Locate and identify every blood parasite.
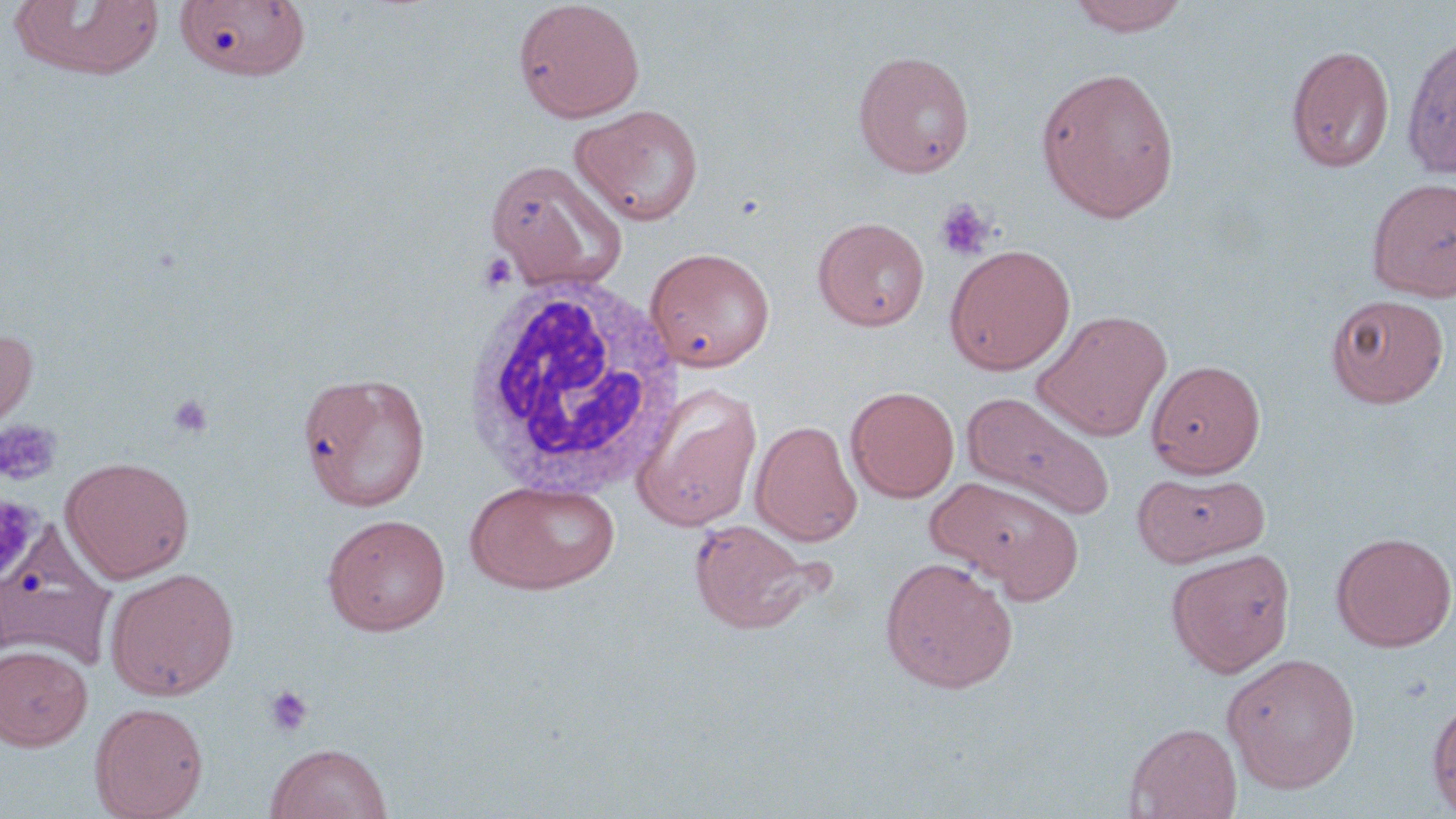
No blood parasites seen.

Approximate bounding boxes as (x1, y1, x2, y2) in pixels. Uninfected red blood cell locations: (1065, 0, 1191, 36), (8, 1, 167, 81), (175, 1, 310, 81), (513, 1, 645, 123), (1400, 32, 1456, 179), (1286, 44, 1395, 172), (852, 50, 975, 178), (1036, 65, 1180, 223), (570, 104, 704, 226), (485, 158, 627, 291), (1366, 177, 1456, 301), (813, 217, 930, 331), (944, 244, 1076, 375), (645, 247, 775, 372), (1326, 293, 1449, 407), (1032, 309, 1173, 441), (0, 326, 38, 439), (1146, 359, 1266, 477), (297, 371, 431, 511), (631, 381, 764, 531), (846, 386, 960, 502), (961, 391, 1114, 521), (751, 420, 862, 546), (61, 456, 195, 582), (1134, 471, 1269, 566), (926, 476, 1082, 596), (465, 479, 620, 595), (321, 513, 451, 636), (689, 518, 825, 635), (0, 520, 117, 671), (1331, 531, 1456, 652), (1165, 548, 1296, 677), (880, 556, 1018, 693), (105, 567, 240, 701), (0, 644, 93, 751), (1222, 652, 1361, 794), (1427, 699, 1456, 816), (89, 701, 209, 819), (1125, 722, 1242, 818), (265, 742, 393, 819). Platelet locations: (935, 199, 995, 261), (476, 252, 518, 295), (166, 394, 215, 439), (0, 418, 62, 486), (264, 685, 314, 736). White blood cell locations: (462, 274, 687, 504). Slide-level diagnosis: negative for blood parasites. Single field of view. Light microscopy. Image is 1456×819 pixels. Captured at 1000x magnification. Thin blood film. May-Grünwald-Giemsa stain.